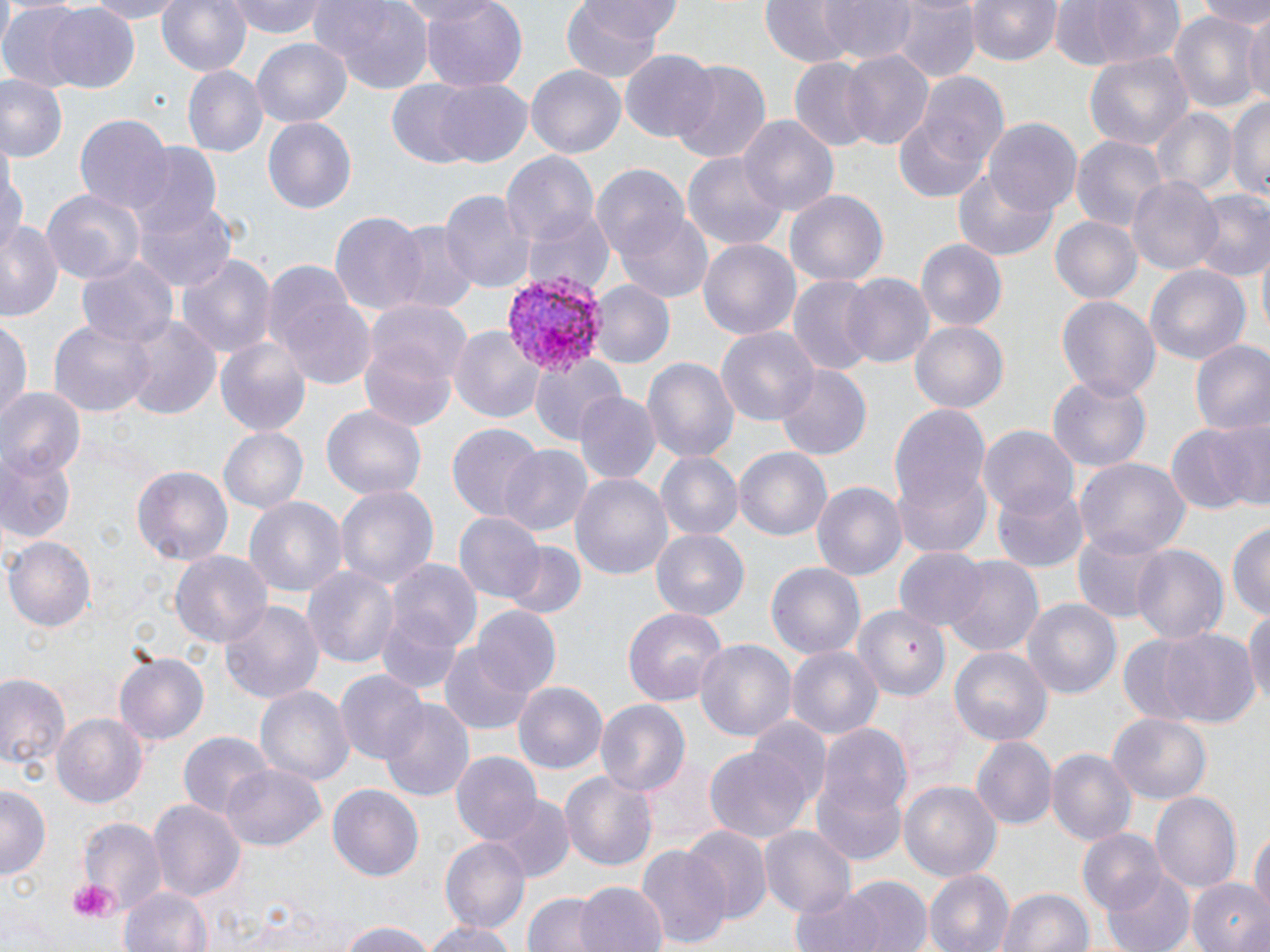
slide-level diagnosis = Plasmodium vivax
modality = optical microscopy
preparation = thin blood film
stain = May-Grünwald-Giemsa
uninfected red blood cell locations = approximate bounding boxes as (x1,y1)-(x2,y2) corner pairs in pixels: (77,0)-(194,22), (155,0)-(253,80), (230,0)-(327,38), (383,0)-(493,25), (415,0)-(531,91), (559,0)-(684,76), (822,0)-(915,64), (964,0)-(1063,65), (1049,0)-(1183,71), (1192,0)-(1270,27), (313,1)-(436,94), (758,1)-(852,68), (893,2)-(977,82), (41,3)-(139,91), (0,4)-(90,92), (1243,7)-(1270,112), (1170,10)-(1263,116), (252,40)-(351,127), (838,48)-(935,150), (1084,50)-(1194,156), (620,51)-(719,143), (789,58)-(876,153), (668,60)-(771,164), (526,64)-(625,157), (184,66)-(265,156), (916,74)-(1009,175), (0,77)-(65,163), (430,81)-(533,169), (384,85)-(490,166), (1229,94)-(1270,207), (891,104)-(996,207), (1151,108)-(1237,199), (74,115)-(174,217), (736,115)-(839,220), (263,117)-(356,214), (984,117)-(1083,217), (1072,134)-(1167,233), (126,143)-(223,234), (0,151)-(26,258), (500,152)-(598,254), (684,152)-(787,255), (953,166)-(1060,262), (591,167)-(693,268), (1128,176)-(1225,275), (40,184)-(148,283), (440,188)-(534,295), (783,189)-(888,288), (1191,189)-(1270,284), (134,196)-(236,293), (522,207)-(615,298), (613,208)-(713,302), (329,211)-(429,319), (1051,215)-(1143,306), (0,220)-(64,321), (393,226)-(477,312), (699,239)-(800,340), (915,239)-(1007,330), (76,253)-(179,349), (177,253)-(276,362), (1146,265)-(1250,366), (266,269)-(376,392), (839,273)-(934,369), (787,276)-(879,380), (589,281)-(674,370), (1055,294)-(1160,403), (362,296)-(470,405), (47,317)-(154,418), (122,317)-(220,417), (909,319)-(1008,412), (0,320)-(31,425), (450,324)-(546,426), (717,326)-(820,430), (359,338)-(458,431), (214,339)-(312,439), (1191,340)-(1270,440), (527,354)-(624,445), (641,355)-(739,465), (770,361)-(873,463), (1048,378)-(1150,472), (0,390)-(83,482), (573,392)-(660,484), (890,402)-(993,537), (322,404)-(426,501), (1213,415)-(1270,511), (1167,422)-(1260,515), (447,424)-(542,522), (978,424)-(1078,519), (218,427)-(307,514), (0,445)-(77,546), (498,445)-(592,539), (735,448)-(830,540), (657,452)-(741,539), (1075,458)-(1191,559), (133,464)-(234,568), (894,465)-(991,558), (571,473)-(673,581), (812,479)-(909,582), (993,483)-(1088,571), (337,486)-(437,591), (244,497)-(347,602), (454,511)-(544,601), (1227,521)-(1270,621), (649,527)-(750,621), (1074,532)-(1170,624), (5,536)-(95,633), (502,542)-(587,622), (1132,544)-(1228,646), (894,546)-(989,633), (169,549)-(275,650), (945,554)-(1043,656), (386,561)-(483,660), (766,561)-(866,660), (303,563)-(399,667), (375,598)-(469,696), (1023,598)-(1122,702), (222,602)-(324,705), (1245,604)-(1270,717), (623,605)-(728,706), (473,606)-(560,697), (851,608)-(947,700), (1148,627)-(1261,729), (694,638)-(798,744), (440,643)-(533,735), (787,645)-(882,741), (949,646)-(1052,747), (114,650)-(210,745), (335,669)-(427,766), (0,674)-(70,772), (514,681)-(608,775), (258,686)-(353,788), (594,697)-(690,798), (378,700)-(474,802), (53,711)-(149,809), (1108,713)-(1213,803), (752,714)-(829,805), (813,720)-(914,852), (179,731)-(272,823), (972,737)-(1055,829), (706,744)-(813,844), (1046,748)-(1137,846), (452,750)-(543,844), (218,763)-(325,852), (561,768)-(658,874), (898,780)-(1002,883), (327,783)-(424,883), (0,785)-(49,882), (1150,789)-(1241,894), (490,795)-(574,883), (149,798)-(243,905), (75,816)-(167,917), (1247,826)-(1269,919), (687,827)-(769,922), (759,827)-(855,915), (1075,831)-(1167,916), (440,837)-(528,934), (638,844)-(730,950), (1102,868)-(1195,952), (923,869)-(1013,952), (837,875)-(933,952), (1186,880)-(1270,952), (575,881)-(665,952), (117,885)-(215,952), (996,885)-(1094,952), (789,886)-(888,952), (522,892)-(606,952), (420,918)-(517,952), (336,920)-(440,952)
image size = 1270×952 pixels
Plasmodium vivax-infected red blood cell locations = approximate bounding boxes as (x1,y1)-(x2,y2) corner pairs in pixels: (502,270)-(604,374)
field of view = one of a larger specimen
magnification = 1000x
platelet locations = approximate bounding boxes as (x1,y1)-(x2,y2) corner pairs in pixels: (66,879)-(118,923)